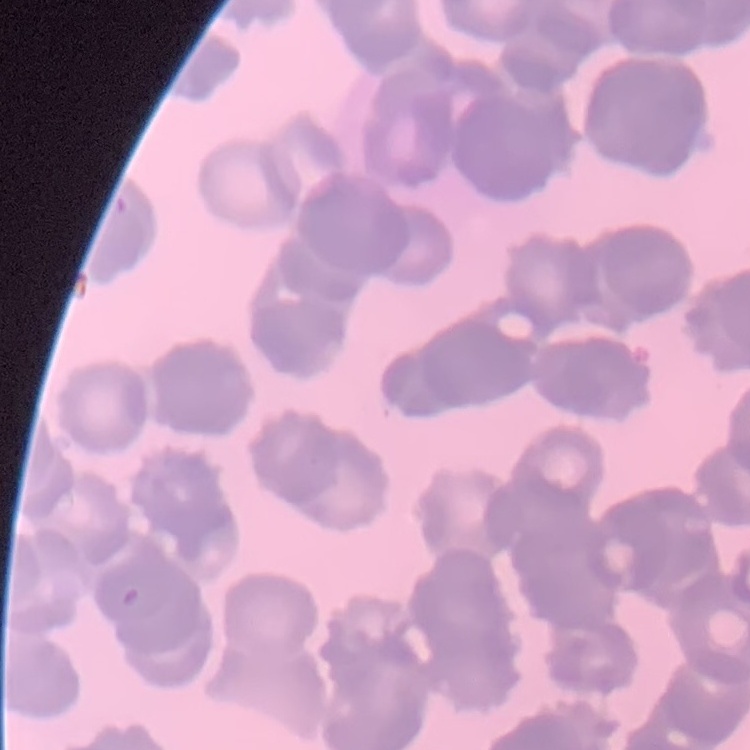

erythrocyte morphology = rouleaux formation
stain = Field's or Giemsa
image type = one tile cut from a larger photomicrograph
preparation = thin peripheral smear